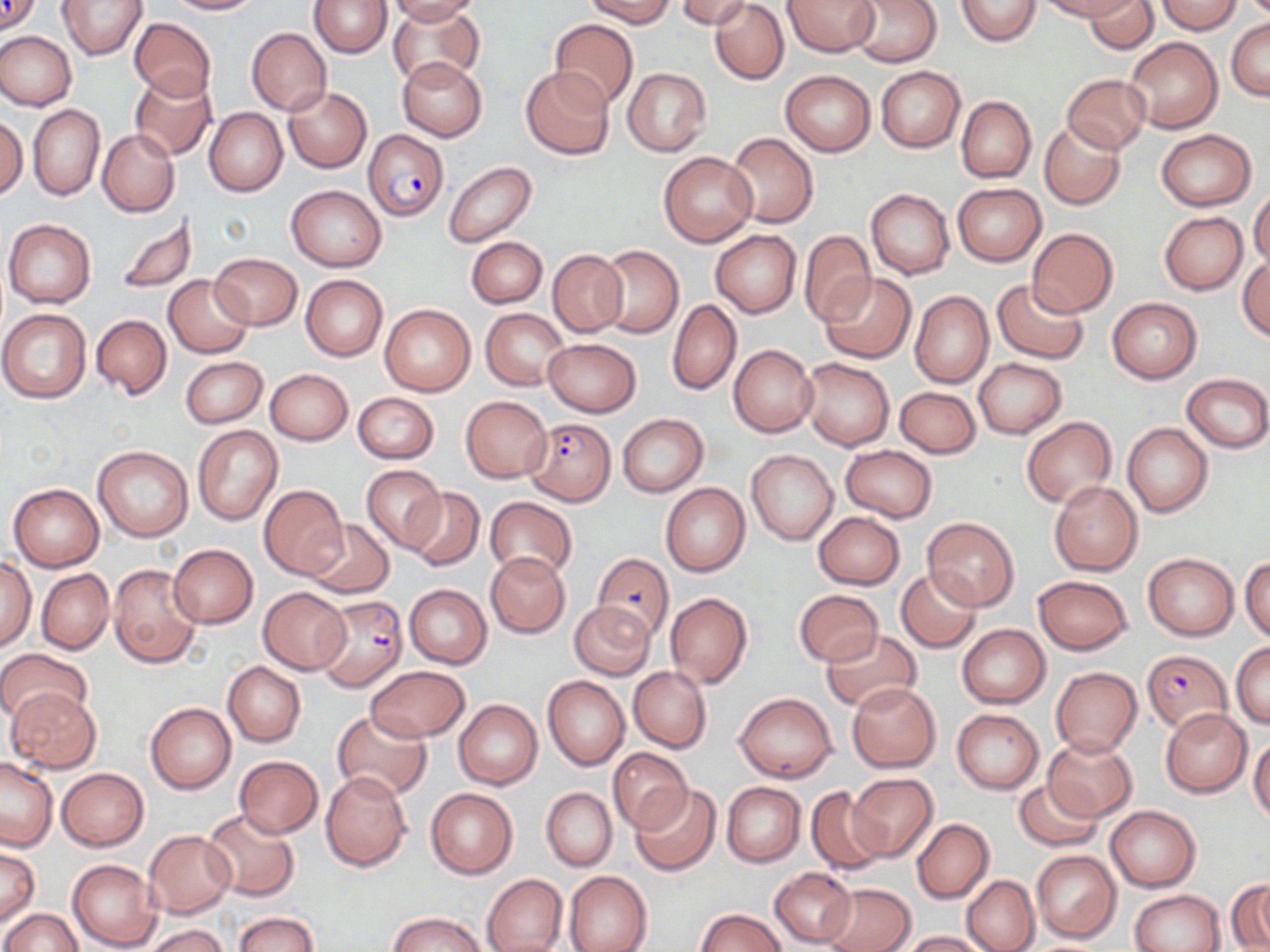

Summary:
  - Coordinate format: approximate bounding boxes as (x1,y1)-(x2,y2) corner pairs in pixels
  - Uninfected red blood cell locations: (0,0)-(41,36), (58,0)-(147,59), (164,0)-(262,15), (309,0)-(392,58), (389,0)-(482,23), (585,0)-(677,27), (677,0)-(752,28), (782,0)-(880,56), (847,0)-(941,67), (955,0)-(1043,47), (1039,0)-(1139,21), (1083,1)-(1156,55), (1156,1)-(1244,34), (387,2)-(485,87), (710,2)-(789,85), (127,17)-(217,104), (549,18)-(639,109), (1226,19)-(1270,100), (247,27)-(331,115), (0,30)-(77,110), (1123,37)-(1223,133), (399,56)-(487,141), (522,66)-(613,160), (876,66)-(964,152), (623,67)-(711,155), (781,71)-(875,157), (130,72)-(217,161), (1062,74)-(1152,153), (283,87)-(371,173), (956,96)-(1036,183), (29,105)-(105,201), (203,107)-(287,196), (1,111)-(27,200), (1040,121)-(1125,209), (97,129)-(180,217), (1157,129)-(1255,211), (725,132)-(818,228), (658,151)-(758,247), (444,161)-(538,247), (953,182)-(1045,265), (287,184)-(386,271), (1249,185)-(1270,269), (865,188)-(954,279), (1159,211)-(1248,294), (113,213)-(198,295), (4,218)-(97,309), (1026,228)-(1119,318), (799,230)-(875,326), (711,231)-(802,317), (466,238)-(547,308), (596,245)-(684,338), (547,249)-(627,338), (210,253)-(302,330), (1237,255)-(1269,342), (819,272)-(916,363), (164,274)-(253,358), (301,274)-(388,362), (992,278)-(1088,364), (909,290)-(993,387), (1107,298)-(1201,383), (667,299)-(740,395), (381,303)-(475,395), (0,307)-(93,403), (480,309)-(567,388), (92,314)-(171,399), (544,338)-(641,416), (728,344)-(818,437), (181,356)-(266,428), (800,357)-(894,450), (974,358)-(1066,438), (264,368)-(354,445), (1182,373)-(1270,451), (895,387)-(981,458), (352,391)-(440,464), (460,395)-(552,484), (618,413)-(708,497), (1021,417)-(1117,508), (1122,423)-(1214,518), (193,425)-(282,524), (93,445)-(193,541), (841,446)-(937,521), (746,450)-(838,544), (361,466)-(446,552), (1049,480)-(1143,575), (660,482)-(750,576), (9,483)-(104,571), (259,484)-(349,579), (404,487)-(484,571), (484,497)-(578,582), (814,511)-(903,589), (922,517)-(1020,611), (304,519)-(394,598), (167,543)-(258,629), (485,552)-(570,638), (1143,553)-(1238,641), (1,556)-(36,651), (1240,556)-(1270,642), (108,564)-(201,668), (37,568)-(113,654), (895,568)-(982,653), (1033,575)-(1133,655), (404,584)-(492,668), (258,587)-(350,675), (793,589)-(883,665), (663,591)-(752,689), (569,600)-(656,681), (957,624)-(1050,708), (819,629)-(921,712), (1232,641)-(1270,730), (0,647)-(91,723), (223,661)-(306,746), (364,665)-(471,742), (629,667)-(711,752), (1051,667)-(1141,756), (543,676)-(630,770), (847,682)-(941,771), (7,688)-(101,773), (734,690)-(838,783), (453,699)-(542,790), (146,702)-(236,793), (952,708)-(1043,793), (1160,708)-(1252,797), (331,710)-(431,801), (1249,735)-(1270,824), (1044,737)-(1137,821), (608,747)-(691,833), (234,755)-(324,838), (0,757)-(58,851), (56,768)-(148,851), (320,770)-(411,872), (846,773)-(938,861), (1014,779)-(1103,851), (722,782)-(805,866), (629,784)-(723,878), (805,785)-(888,876), (425,786)-(518,879), (541,787)-(616,871), (1105,805)-(1200,891), (204,809)-(300,900), (912,818)-(994,904), (144,829)-(237,916), (1,845)-(39,926), (1031,849)-(1121,943), (67,858)-(161,950), (768,868)-(856,948), (564,870)-(653,952), (482,873)-(567,952), (962,875)-(1039,952), (1227,881)-(1270,952), (821,882)-(914,952), (1129,888)-(1224,952), (695,908)-(785,952), (3,909)-(82,952), (233,911)-(319,952), (387,912)-(491,952), (142,924)-(230,952), (899,930)-(993,951)
  - Plasmodium falciparum-infected red blood cell locations: (363,129)-(447,222), (524,418)-(616,505), (588,554)-(673,638), (316,595)-(409,691), (1142,651)-(1232,735)
  - Slide-level diagnosis: Plasmodium falciparum
  - Image size: 1270×952 pixels
  - Modality: optical microscopy
  - Stain: May-Grünwald-Giemsa
  - Field of view: one of a larger specimen
  - Magnification: 1000x
  - Preparation: thin blood smear